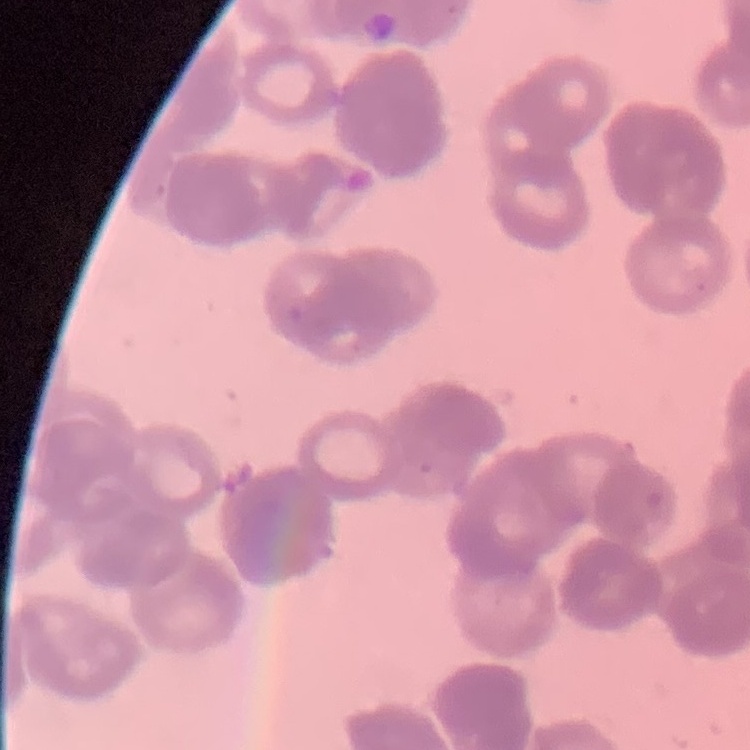
{
  "erythrocyte_morphology": "rouleaux formation",
  "image_type": "square crop of a larger photomicrograph",
  "preparation": "thin blood smear",
  "stain": "Field's or Giemsa"
}